Locate and identify every blood parasite.
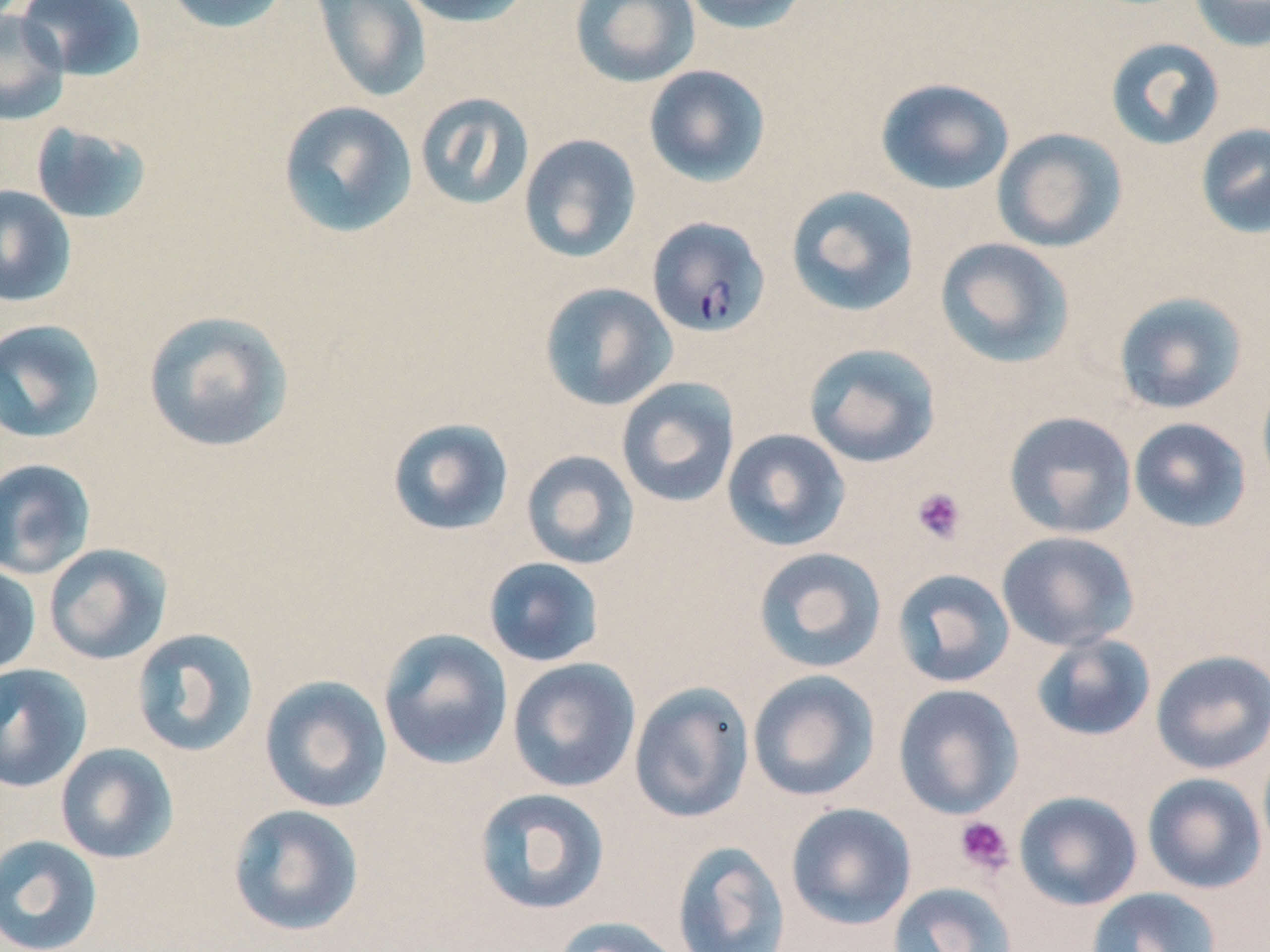

Approximate bounding boxes as [x1, y1, x2, y2] in pixels.
Plasmodium falciparum-infected red blood cells: [647, 216, 771, 338].
No Plasmodium ovale, Plasmodium malariae, Plasmodium vivax, Babesia divergens, or Trypanosoma brucei observed.

Summary:
  - Platelet locations (subset): [911, 487, 967, 544], [954, 816, 1014, 876]
  - Uninfected red blood cell locations (subset): [15, 0, 146, 81], [161, 0, 292, 34], [310, 0, 433, 104], [396, 0, 534, 28], [570, 0, 700, 88], [679, 0, 813, 35], [1188, 0, 1270, 51], [0, 7, 69, 126], [1105, 36, 1225, 151], [643, 65, 771, 187], [875, 78, 1014, 195], [414, 91, 535, 211], [277, 100, 418, 239], [30, 121, 152, 225], [1196, 122, 1270, 239], [992, 128, 1127, 252], [518, 134, 642, 263], [0, 185, 77, 309], [785, 185, 921, 318], [935, 237, 1075, 369], [538, 282, 677, 411], [1113, 291, 1248, 415], [142, 310, 295, 453], [0, 318, 106, 444], [803, 342, 942, 468], [1256, 374, 1270, 498], [615, 377, 741, 508], [1003, 410, 1137, 539], [386, 417, 515, 537], [1128, 417, 1253, 533], [721, 428, 851, 551], [520, 450, 640, 570], [0, 458, 96, 579], [997, 530, 1139, 652], [43, 543, 173, 665], [752, 547, 887, 673], [483, 557, 605, 668], [0, 561, 41, 677], [892, 568, 1016, 688], [130, 628, 259, 758], [378, 628, 513, 770], [1031, 632, 1157, 742], [1151, 649, 1270, 774], [507, 657, 641, 793], [0, 662, 92, 793], [747, 670, 881, 802], [259, 674, 393, 814], [629, 681, 755, 824], [55, 743, 178, 864], [1142, 773, 1267, 894], [473, 787, 611, 916], [1013, 791, 1143, 911], [785, 802, 917, 929], [227, 803, 365, 937], [0, 834, 103, 952], [672, 840, 790, 952], [888, 882, 1018, 952], [1085, 887, 1222, 952], [552, 916, 683, 952]
  - Slide-level diagnosis: Plasmodium falciparum
  - Magnification: 1000x
  - Field of view: single
  - Stain: May-Grünwald-Giemsa
  - Image size: 1270×952 pixels
  - Modality: optical microscopy
  - Preparation: thin blood smear